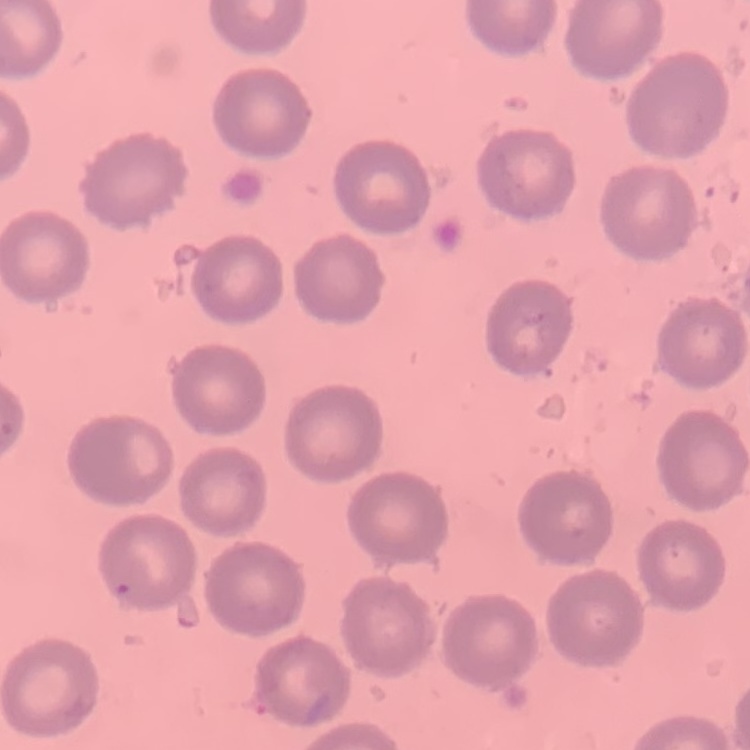

The erythrocytes exhibit no rouleaux formation. Stained with either Field's or Giemsa. Thin blood film. One tile cut from a larger photomicrograph.